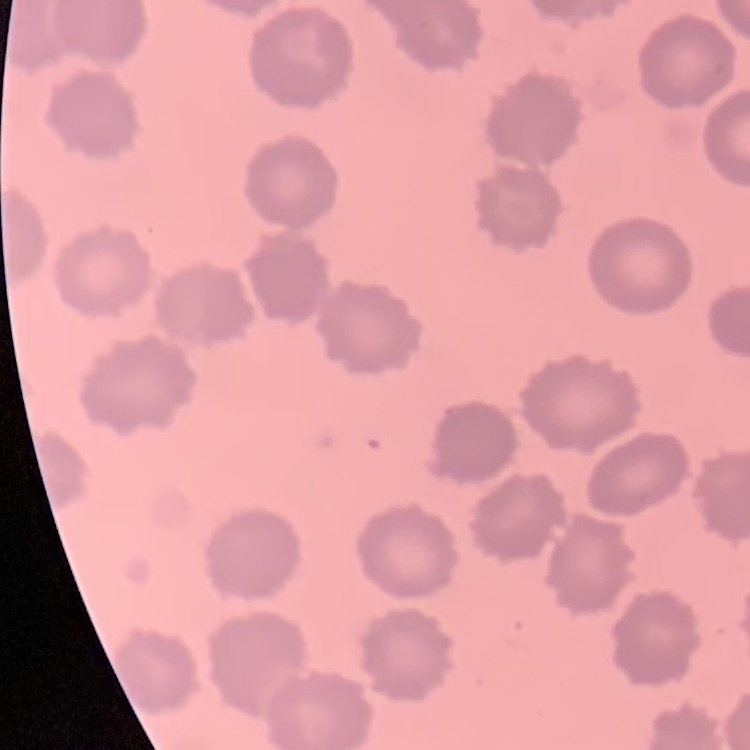
red blood cell morphology = no rouleaux formation
stain = Field's or Giemsa
preparation = thin blood smear
image type = one tile cut from a larger photomicrograph